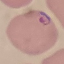

malaria status = parasitized
capture = smartphone camera at the microscope eyepiece
preparation = thin blood film
stain = Giemsa
image type = cell patch, automatically extracted from a larger field of view and resized to 64 × 64 pixels